Describe the morphology of the erythrocytes.
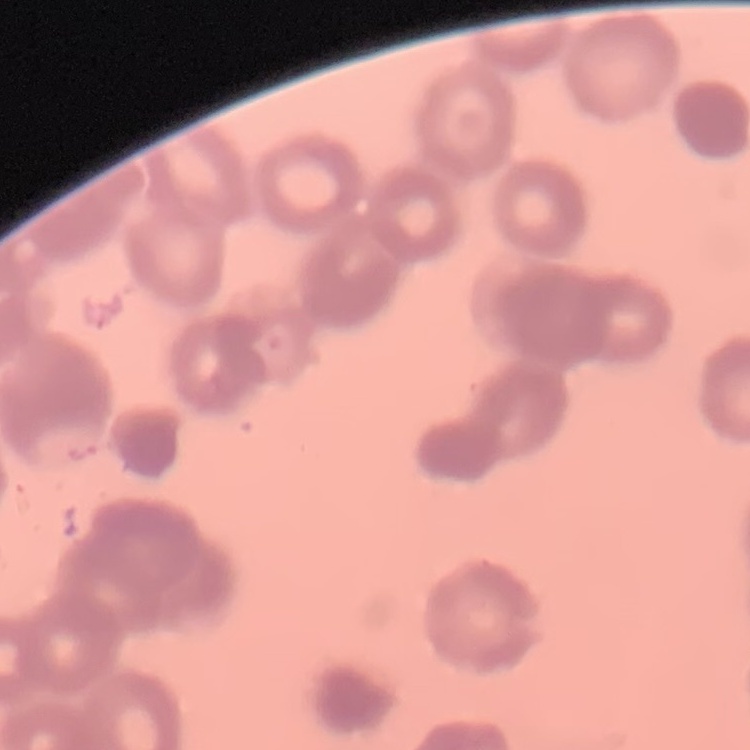

They show rouleaux formation.

Thin peripheral smear. Field's or Giemsa stain. One tile cut from a larger photomicrograph.